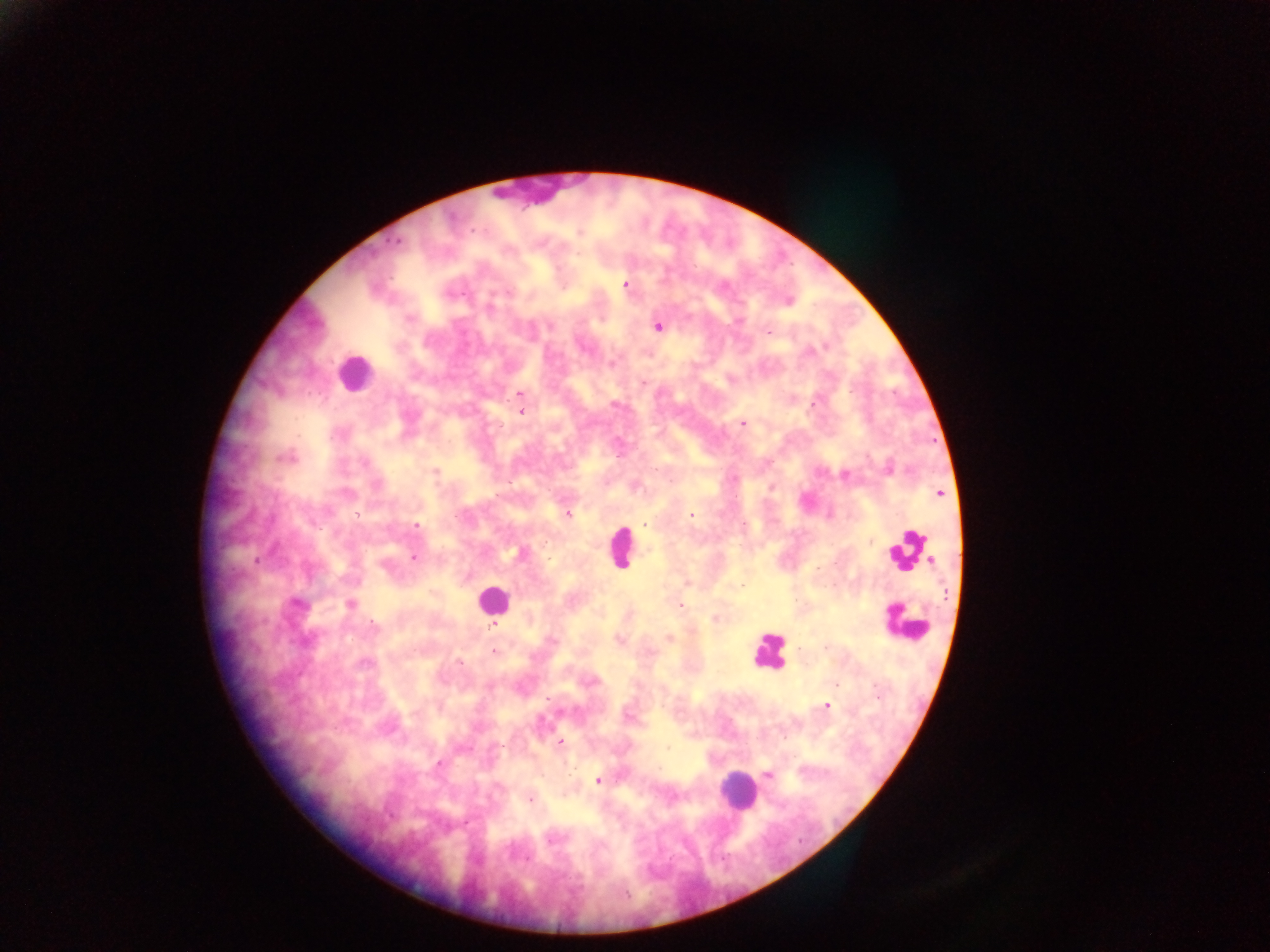

Approximate centers as {x, y} in pixels.
Summary:
  - Malaria parasite locations: {396, 241}, {626, 285}, {725, 286}, {788, 301}, {489, 309}, {549, 326}, {658, 326}, {768, 332}, {824, 345}, {613, 364}, {643, 383}, {520, 394}, {614, 404}, {812, 404}, {522, 411}, {742, 423}, {286, 458}, {363, 462}, {436, 471}, {845, 474}, {940, 493}, {356, 514}, {569, 515}, {691, 515}, {456, 517}, {416, 525}, {645, 525}, {414, 557}, {257, 561}, {298, 604}, {351, 605}, {680, 605}, {715, 619}, {375, 624}, {494, 626}, {670, 638}, {620, 640}, {494, 652}, {459, 661}, {364, 664}, {836, 684}, {547, 698}, {827, 705}, {628, 717}, {560, 743}, {501, 746}, {668, 747}, {439, 764}, {768, 775}, {597, 780}, {530, 799}, {552, 840}, {626, 894}
  - Leukocyte locations: {353, 373}, {620, 548}, {910, 550}, {493, 597}, {905, 622}, {769, 651}, {736, 790}
  - Preparation: thick blood film
  - Field of view: single
  - Country: Ghana
  - Capture: mobile-phone photograph through a microscope
  - Image size: 1270×952 pixels